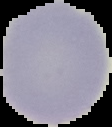
Result: no malaria parasites detected. From a thin blood film. Image is 112×127 pixels. Segmented cell region on a black background.